Draw a bounding box around every parasitised red blood cell, every trophozoite, every gametocyte, every leukocyte, and every artifact (platelet-like body, stain precipitate, or debris).
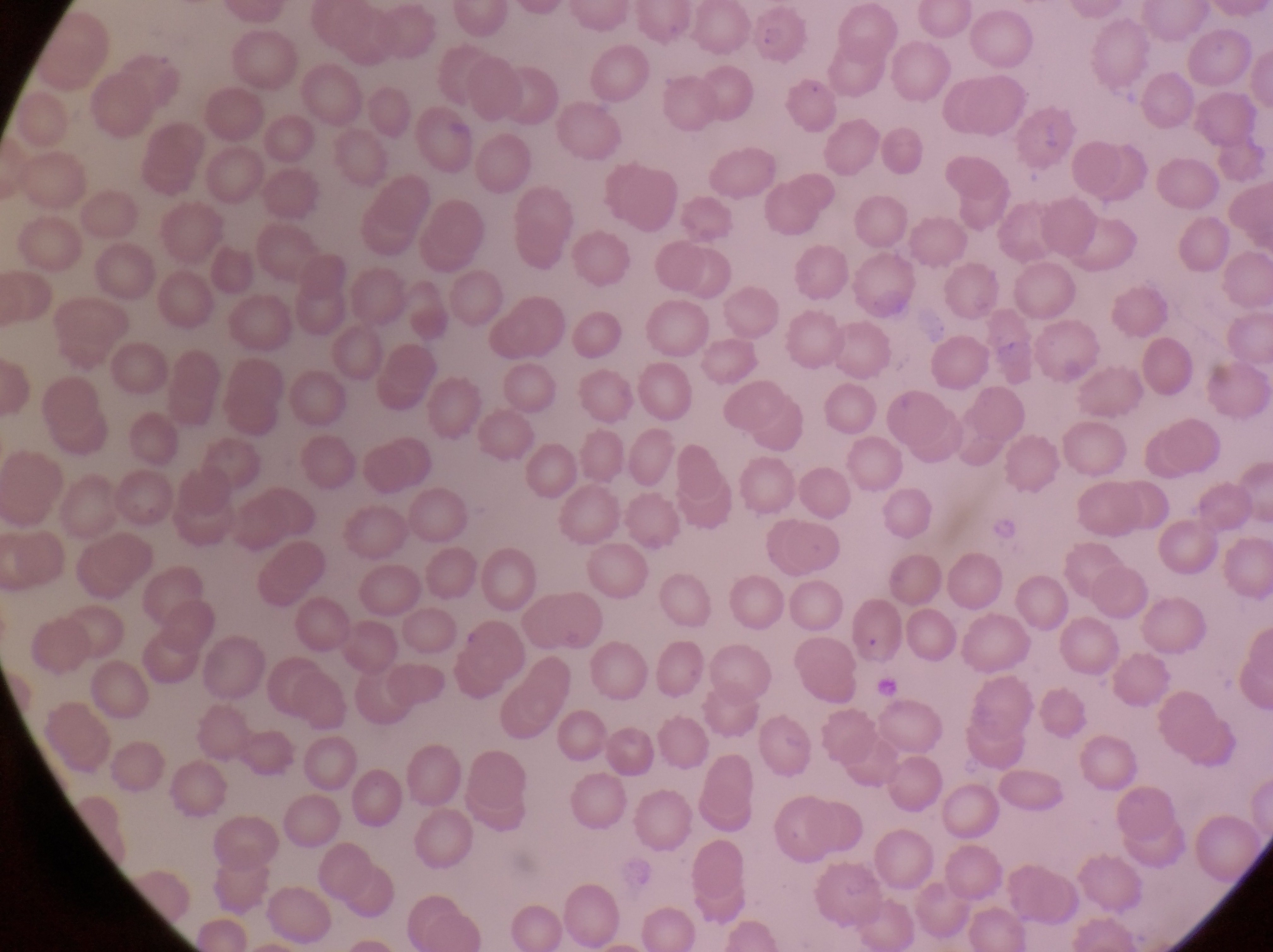

Approximate bounding boxes as left top right bottom in pixels.
Trophozoites: 983 510 1023 553.
No leukocytes observed.
Artifacts (platelet-like body, stain precipitate, or debris): 876 672 904 702.

Summary:
  - Magnification: 1000x
  - Preparation: thin blood smear
  - Image size: 1273×952 pixels
  - Field of view: single
  - Capture: smartphone photograph through the eyepiece of an Olympus CX-23 microscope
  - Country: Uganda